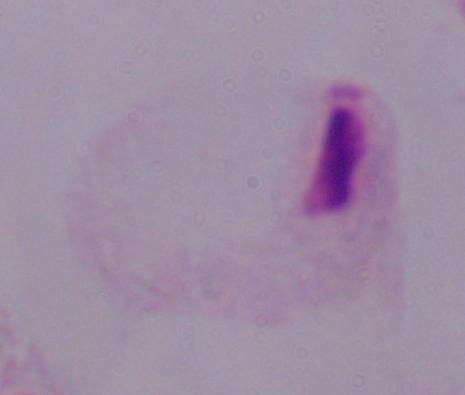 Captured at 1000x magnification. Photomicrograph. A trichomonad is seen.